Identify the blood parasite species.
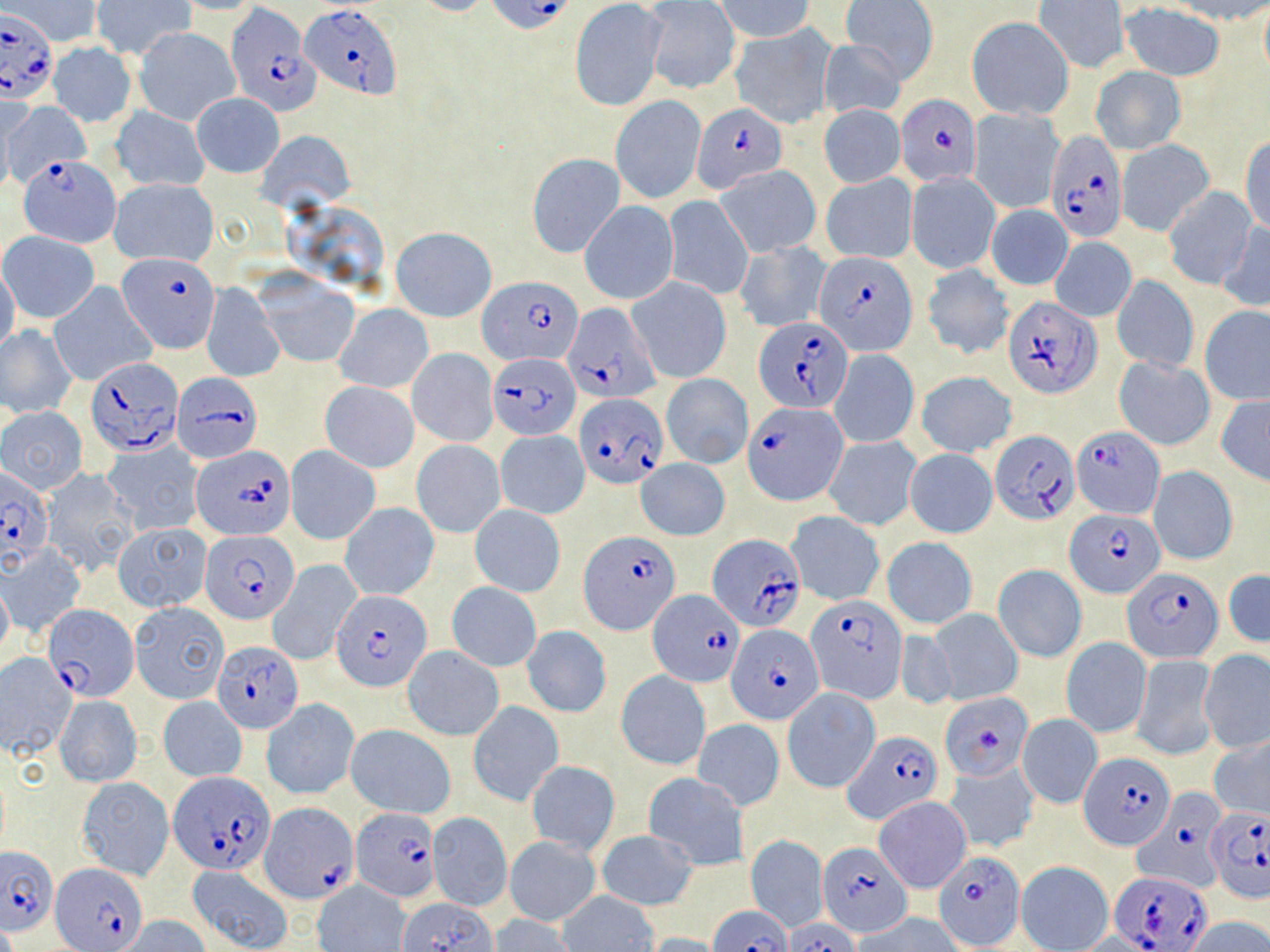

Plasmodium falciparum.

Summary:
  - Coordinate format: approximate bounding boxes as (x1,y1)-(x2,y2) corner pairs in pixels
  - Plasmodium falciparum-infected red blood cell locations (subset): (486,0)-(570,32), (301,3)-(401,98), (227,6)-(315,116), (0,7)-(57,104), (895,95)-(982,186), (1046,134)-(1129,241), (20,157)-(122,247), (117,251)-(221,354), (816,252)-(918,356), (479,279)-(582,366), (1005,296)-(1100,398), (564,303)-(659,404), (755,319)-(851,412), (488,352)-(581,439), (86,357)-(184,457), (171,371)-(262,462), (574,392)-(669,489), (745,402)-(844,504), (1071,425)-(1163,520), (990,428)-(1079,525), (192,444)-(298,538), (0,469)-(55,570), (1068,512)-(1166,595), (200,529)-(299,624), (581,530)-(674,632), (707,532)-(802,633), (1123,568)-(1223,661), (331,590)-(433,691), (647,590)-(744,687), (806,595)-(907,703), (43,604)-(139,701), (727,623)-(823,724), (941,691)-(1030,781), (842,731)-(944,824), (1082,753)-(1172,849), (170,772)-(275,874), (1134,785)-(1227,895), (261,800)-(357,903), (1205,806)-(1270,901), (352,807)-(439,901), (819,841)-(911,937), (0,845)-(56,935), (933,850)-(1026,949), (51,863)-(146,952), (1112,870)-(1212,949), (710,904)-(791,952), (782,919)-(860,952)
  - Uninfected red blood cell locations (subset): (6,0)-(101,47), (164,0)-(266,15), (402,0)-(499,16), (717,0)-(813,41), (1034,0)-(1127,72), (1162,0)-(1270,25), (93,1)-(193,61), (570,1)-(668,112), (840,1)-(939,82), (643,2)-(740,95), (1118,3)-(1226,80), (966,16)-(1074,121), (730,23)-(837,129), (134,27)-(239,126), (817,39)-(906,120), (47,42)-(138,128), (1090,66)-(1186,155), (191,92)-(284,177), (610,95)-(706,204), (3,101)-(88,186), (0,102)-(14,197), (819,105)-(904,188), (111,106)-(210,192), (968,108)-(1064,214), (258,130)-(355,209), (1241,136)-(1270,237), (1117,140)-(1214,236), (526,153)-(625,259), (1135,161)-(1244,268), (716,165)-(820,256), (907,172)-(1000,275), (821,173)-(917,263), (110,178)-(219,267), (1163,187)-(1258,290), (663,195)-(754,301), (580,200)-(678,304), (985,203)-(1074,290), (1217,219)-(1270,314), (391,227)-(496,322), (1,231)-(100,323), (1050,236)-(1136,322), (735,240)-(832,332), (921,263)-(1013,359), (0,264)-(21,360), (256,274)-(360,367), (1112,274)-(1199,373), (628,277)-(731,384), (49,281)-(155,387), (201,282)-(283,383), (335,303)-(432,392), (1200,306)-(1270,406), (0,324)-(79,419), (407,348)-(497,448), (830,350)-(919,448), (1114,354)-(1216,450), (916,371)-(1018,457), (661,373)-(752,468), (320,381)-(419,472), (1216,395)-(1270,486), (1,405)-(88,494), (495,430)-(590,519), (823,435)-(921,530), (102,440)-(203,533), (411,440)-(505,538), (285,447)-(380,545), (904,449)-(997,538), (637,458)-(730,540), (1148,466)-(1239,566), (38,468)-(138,576), (340,503)-(436,600), (469,504)-(566,597), (786,512)-(884,605), (114,523)-(210,612), (882,537)-(977,629), (1,545)-(85,637), (268,561)-(362,666), (993,564)-(1086,662), (1224,569)-(1270,649), (0,576)-(12,661), (446,581)-(541,671), (129,602)-(228,705), (928,608)-(1022,705), (523,627)-(611,717), (893,627)-(958,712), (1061,637)-(1151,737), (403,646)-(503,740), (1199,651)-(1269,753), (0,653)-(76,759), (1132,654)-(1218,760), (617,671)-(711,770), (782,688)-(878,793), (55,695)-(143,787), (158,697)-(247,781), (262,699)-(359,799), (469,701)-(562,807), (1017,714)-(1102,808), (693,718)-(785,811), (346,723)-(455,818), (1208,736)-(1270,823), (526,761)-(618,854), (944,761)-(1038,853), (642,772)-(749,870), (77,777)-(174,880), (874,796)-(972,892), (427,811)-(512,912), (597,831)-(699,910), (745,835)-(827,931), (505,836)-(601,926), (1016,861)-(1112,952), (188,865)-(295,952), (313,882)-(410,952), (555,891)-(660,952), (396,898)-(501,952), (856,914)-(965,952), (490,915)-(574,952), (117,916)-(210,952), (1184,916)-(1270,951), (644,933)-(731,952)
  - Image size: 1270×952 pixels
  - Preparation: thin blood film
  - Magnification: 1000x
  - Modality: optical microscopy
  - Field of view: one of a larger specimen
  - Stain: May-Grünwald-Giemsa